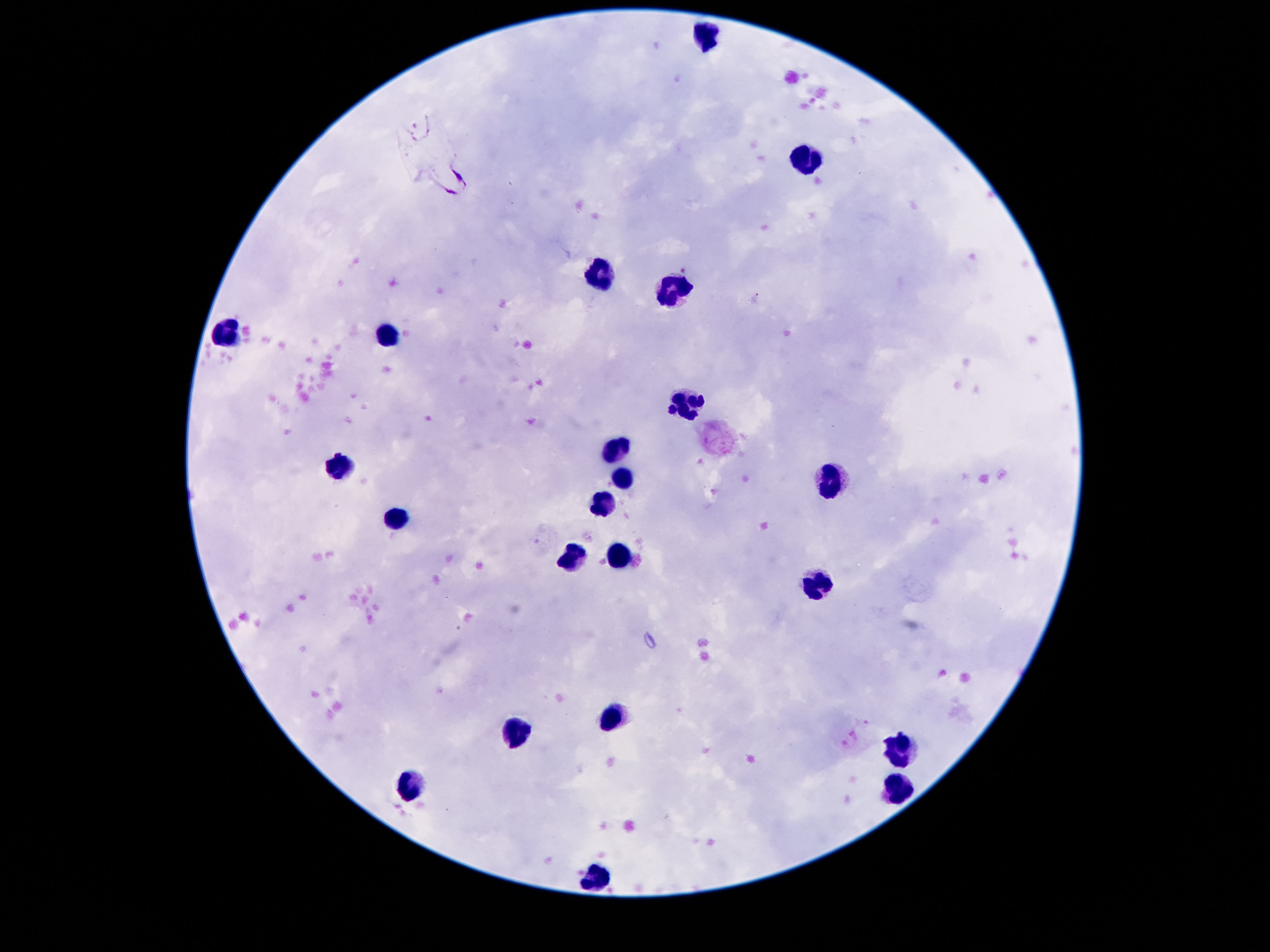

Approximate centers as {x, y} in pixels. Leukocyte locations: {706, 37}, {805, 161}, {599, 274}, {675, 287}, {228, 336}, {385, 336}, {688, 405}, {617, 455}, {338, 468}, {626, 479}, {832, 481}, {604, 504}, {396, 519}, {613, 555}, {573, 556}, {818, 579}, {610, 714}, {513, 738}, {900, 749}, {898, 786}, {409, 787}, {595, 878}. Patient malaria status: negative. Photographed through the microscope eyepiece with a smartphone camera. 100x magnification. Giemsa-stained preparation. Single field of view. Thick peripheral-blood smear. Image is 1270×952 pixels.